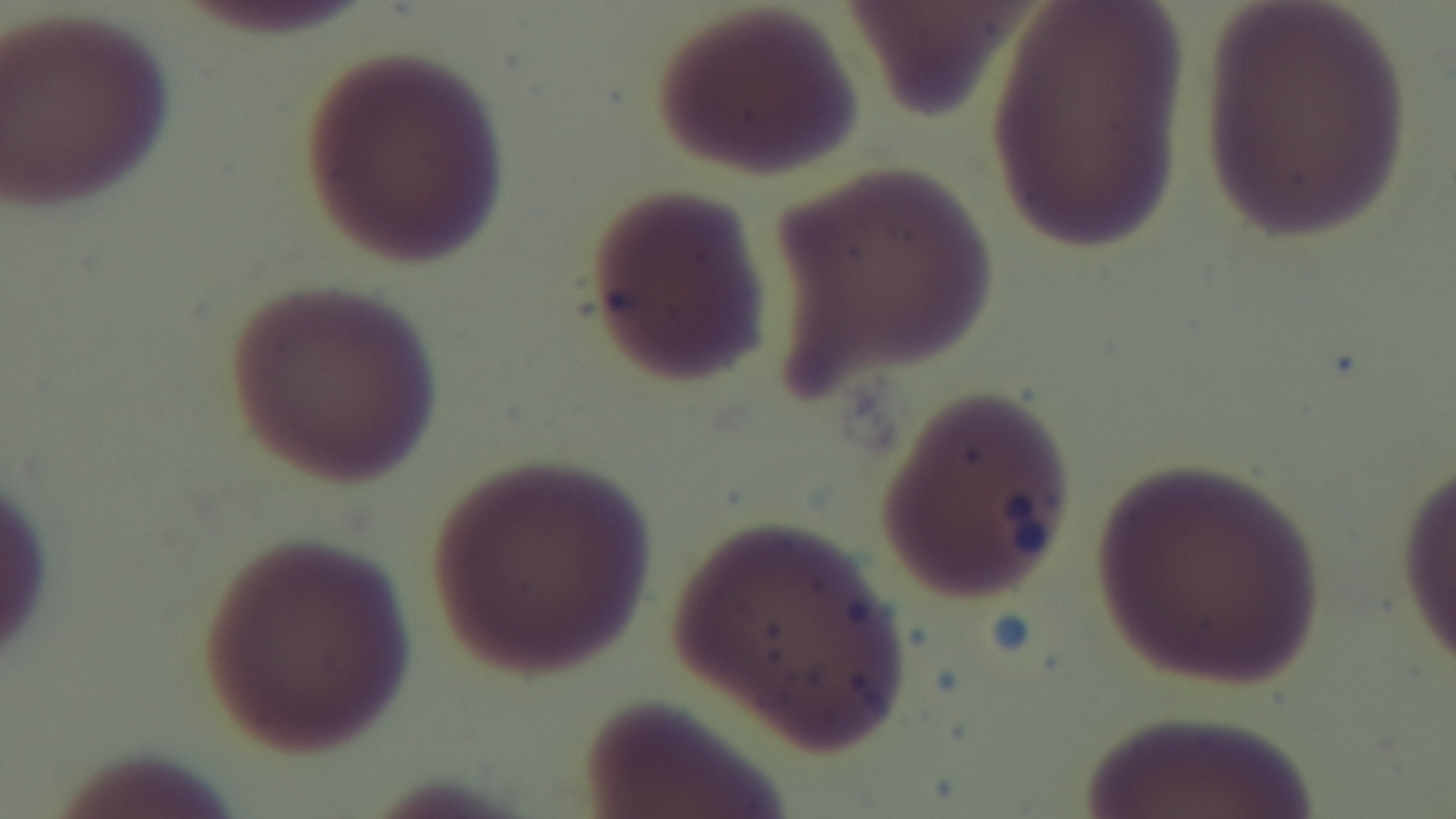 Light microscopy. 100x oil-immersion objective. Preparation: thin smear. Captured with a mounted 4K digital camera. Giemsa stain. One field from the slide. Malaria status: negative.